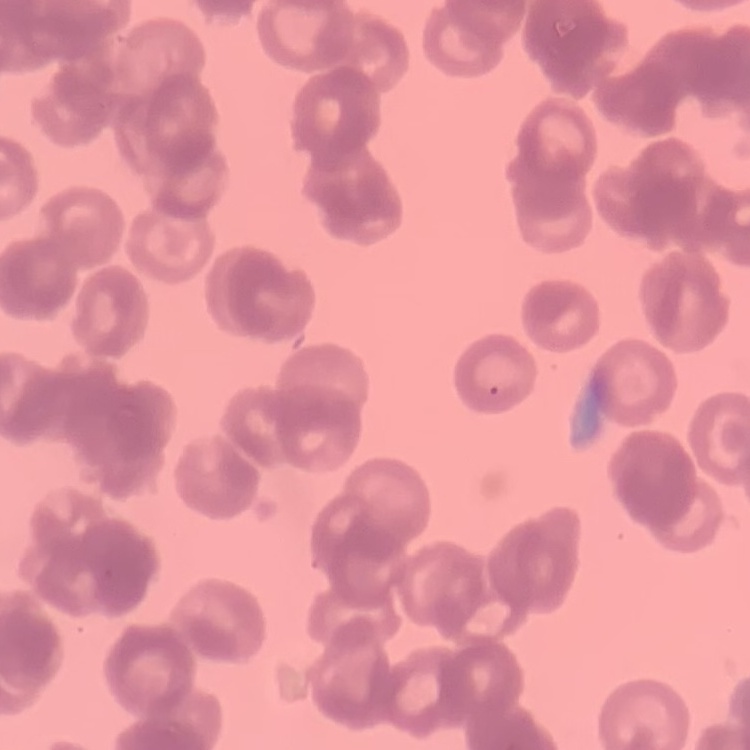
Summary:
  - Red blood cell morphology: rouleaux formation
  - Stain: Field's or Giemsa
  - Image type: one tile cut from a larger photomicrograph
  - Preparation: thin blood film